Locate and identify every blood parasite.
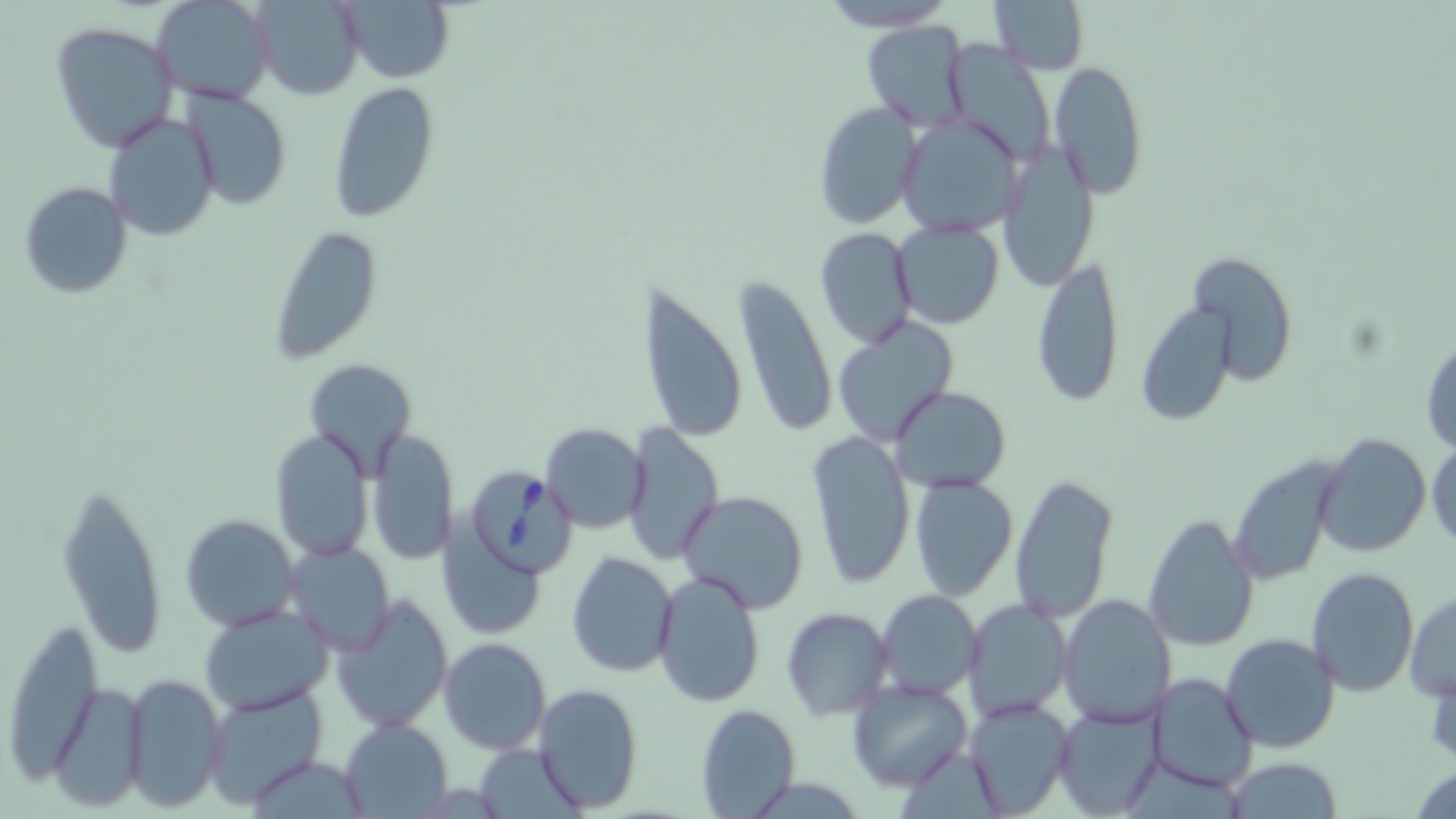
Approximate bounding boxes as [x1, y1, x2, y2] in pixels.
Babesia divergens-infected red blood cells: [464, 466, 577, 578].
No Plasmodium falciparum, Plasmodium ovale, Plasmodium malariae, Plasmodium vivax, or Trypanosoma brucei observed.

Uninfected red blood cell locations: [151, 0, 275, 107], [334, 0, 455, 83], [813, 0, 959, 33], [987, 0, 1089, 75], [250, 1, 364, 100], [862, 21, 971, 130], [50, 23, 177, 152], [1049, 63, 1148, 197], [328, 81, 440, 223], [182, 86, 291, 210], [812, 102, 920, 229], [103, 109, 220, 241], [896, 113, 1022, 238], [995, 143, 1100, 292], [17, 181, 133, 299], [892, 220, 1004, 330], [266, 225, 382, 364], [813, 227, 918, 349], [1032, 251, 1125, 407], [1187, 251, 1297, 387], [732, 276, 838, 440], [638, 282, 748, 446], [1137, 301, 1237, 425], [832, 317, 959, 447], [1421, 334, 1455, 454], [303, 360, 415, 472], [890, 385, 1012, 494], [540, 423, 648, 531], [621, 423, 723, 563], [366, 427, 458, 567], [268, 429, 374, 563], [805, 430, 915, 590], [1312, 434, 1431, 559], [1426, 439, 1456, 550], [1228, 453, 1345, 587], [1010, 471, 1117, 625], [56, 476, 169, 660], [908, 476, 1019, 602], [676, 490, 810, 613], [1143, 512, 1260, 651], [178, 513, 300, 633], [440, 517, 543, 639], [286, 542, 394, 654], [567, 551, 678, 677], [1307, 566, 1419, 696], [652, 570, 767, 707], [876, 590, 982, 699], [1405, 590, 1455, 701], [332, 593, 453, 734], [1058, 595, 1176, 728], [961, 599, 1072, 723], [199, 606, 334, 715], [780, 607, 893, 721], [3, 617, 102, 782], [1221, 633, 1340, 752], [439, 638, 552, 755], [1147, 672, 1260, 794], [122, 673, 226, 809], [845, 677, 972, 791], [46, 683, 147, 811], [533, 683, 644, 814], [203, 686, 327, 808], [964, 697, 1075, 817], [695, 704, 802, 818], [1052, 704, 1166, 819], [338, 719, 452, 816], [474, 743, 582, 816], [1222, 758, 1346, 817]. Slide-level diagnosis: Babesia divergens. Captured at 1000x magnification. Image is 1456×819 pixels. May-Grünwald-Giemsa-stained preparation. Optical microscopy. Single field of view. Thin blood film.